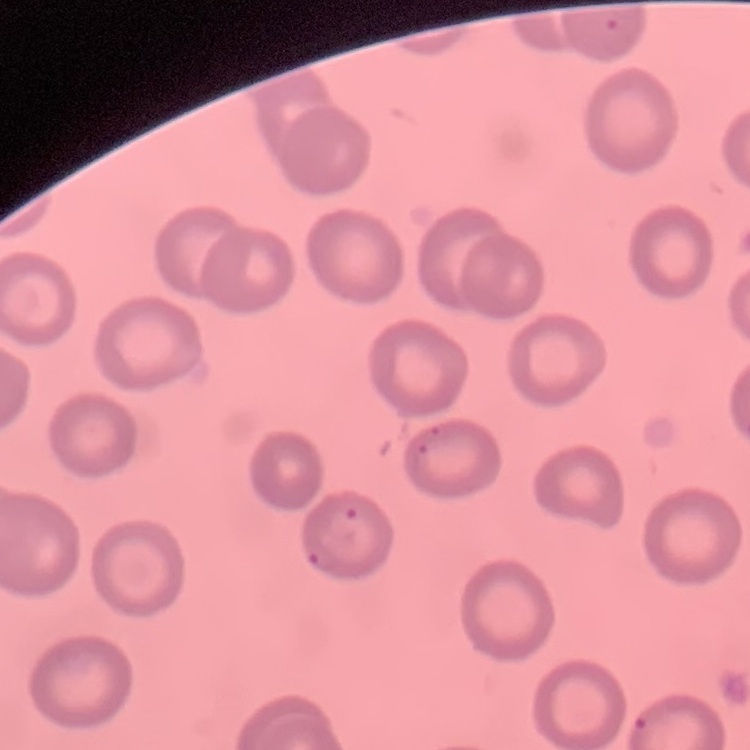 The red blood cells exhibit no rouleaux formation. Thin blood smear. Stained with either Field's or Giemsa. One tile cut from a larger photomicrograph.